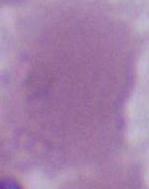

Summary:
  - Modality: micrograph
  - Magnification: 1000x
  - Identification: red blood cell